Describe the morphology of the red blood cells.
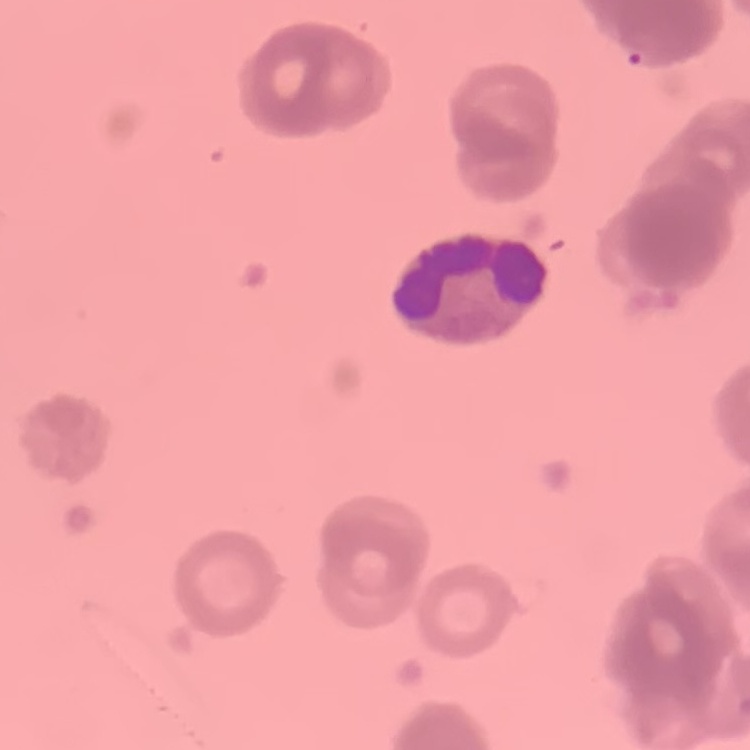
Rouleaux formation.

stain: Field's or Giemsa
preparation: thin blood smear
image_type: square crop of a larger photomicrograph